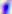

Summary:
  - Modality: photomicrograph
  - Identification: Toxoplasma gondii
  - Magnification: 400x